Report the malaria status of this cell.
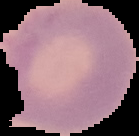

Uninfected.

Summary:
  - Image size: 139×136 pixels
  - Image type: segmented cell region on a black background
  - Preparation: thin blood smear